State which parasite is depicted.
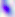
Toxoplasma gondii.

Summary:
  - Magnification: 400x
  - Modality: micrograph